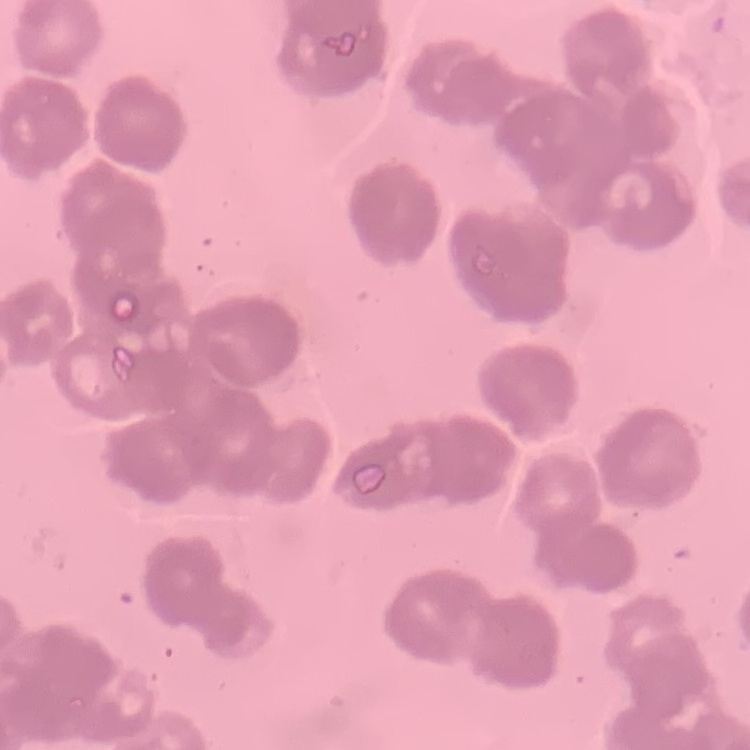
Summary:
  - Erythrocyte morphology: rouleaux formation
  - Stain: Field's or Giemsa
  - Image type: square crop of a larger photomicrograph
  - Preparation: thin blood smear